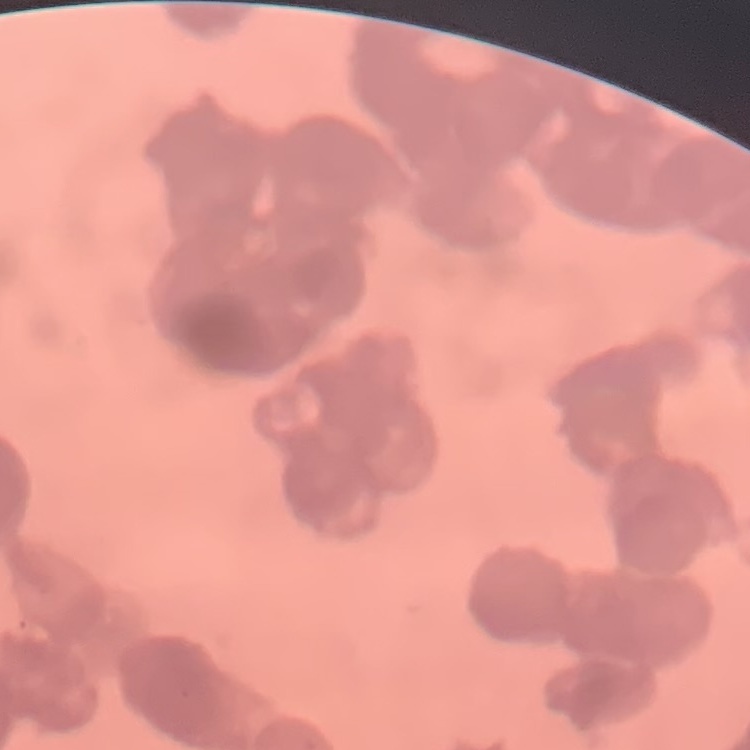 The red blood cells exhibit rouleaux formation. Stained with either Field's or Giemsa. Square crop of a larger photomicrograph. Thin peripheral smear.